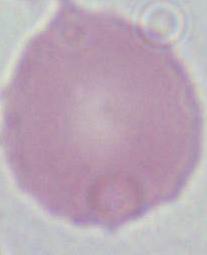

Summary:
  - Magnification: 1000x
  - Modality: micrograph
  - Identification: red blood cell